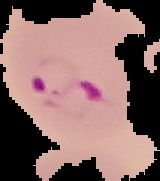
Segmented cell region on a black background. Image is 160×181 pixels. Malaria status: parasitized. From a thin blood film.